Locate every blood parasite and identify its species.
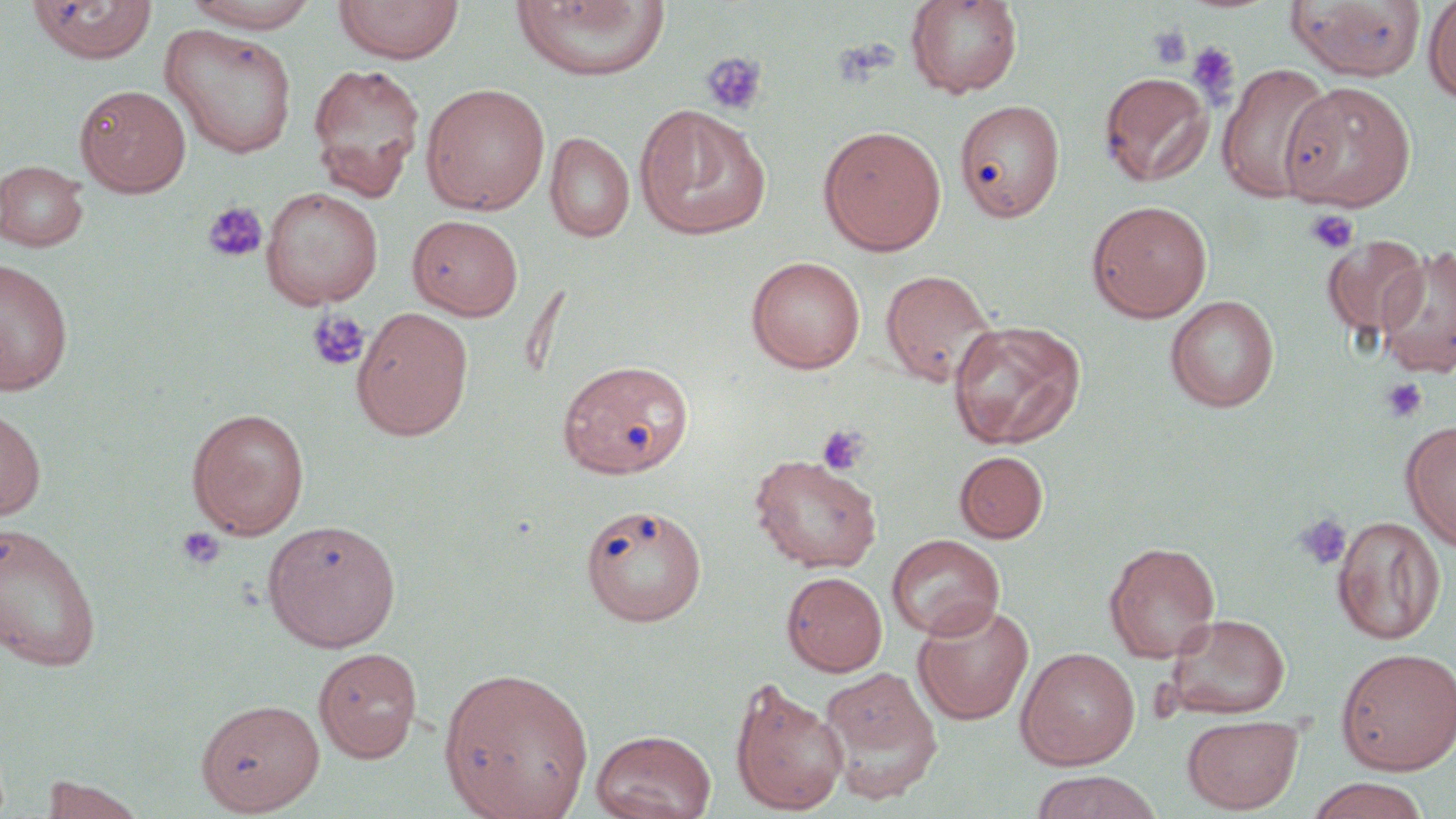

No blood parasites seen.

Summary:
  - Coordinate format: approximate bounding boxes as named x1/y1/x2/y2 corners in pixels
  - Uninfected red blood cell locations: (x1=28, y1=0, x2=157, y2=63), (x1=182, y1=0, x2=323, y2=32), (x1=332, y1=0, x2=464, y2=63), (x1=906, y1=0, x2=1022, y2=99), (x1=1287, y1=0, x2=1427, y2=81), (x1=511, y1=1, x2=670, y2=81), (x1=1423, y1=1, x2=1456, y2=103), (x1=159, y1=23, x2=299, y2=159), (x1=307, y1=62, x2=426, y2=199), (x1=1217, y1=63, x2=1336, y2=202), (x1=1099, y1=72, x2=1214, y2=187), (x1=1280, y1=81, x2=1416, y2=211), (x1=421, y1=83, x2=550, y2=216), (x1=75, y1=84, x2=191, y2=197), (x1=954, y1=99, x2=1065, y2=221), (x1=634, y1=105, x2=771, y2=240), (x1=818, y1=125, x2=947, y2=256), (x1=545, y1=131, x2=635, y2=243), (x1=0, y1=159, x2=90, y2=252), (x1=261, y1=187, x2=384, y2=309), (x1=1086, y1=199, x2=1212, y2=322), (x1=408, y1=214, x2=523, y2=320), (x1=1322, y1=235, x2=1428, y2=341), (x1=1376, y1=247, x2=1456, y2=379), (x1=746, y1=256, x2=866, y2=374), (x1=0, y1=257, x2=74, y2=397), (x1=879, y1=268, x2=999, y2=389), (x1=1165, y1=294, x2=1280, y2=412), (x1=352, y1=306, x2=474, y2=441), (x1=949, y1=320, x2=1086, y2=450), (x1=558, y1=359, x2=694, y2=479), (x1=0, y1=405, x2=46, y2=523), (x1=187, y1=407, x2=310, y2=538), (x1=1401, y1=419, x2=1456, y2=551), (x1=954, y1=451, x2=1048, y2=543), (x1=748, y1=453, x2=883, y2=574), (x1=581, y1=502, x2=707, y2=626), (x1=1332, y1=515, x2=1445, y2=645), (x1=262, y1=518, x2=402, y2=652), (x1=0, y1=520, x2=103, y2=671), (x1=887, y1=534, x2=1005, y2=640), (x1=1104, y1=542, x2=1220, y2=662), (x1=781, y1=571, x2=888, y2=676), (x1=912, y1=602, x2=1035, y2=726), (x1=1164, y1=613, x2=1291, y2=720), (x1=313, y1=646, x2=422, y2=763), (x1=1015, y1=646, x2=1140, y2=769), (x1=1335, y1=647, x2=1456, y2=775), (x1=439, y1=665, x2=595, y2=819), (x1=819, y1=666, x2=942, y2=802), (x1=730, y1=677, x2=849, y2=815), (x1=195, y1=698, x2=325, y2=815), (x1=1182, y1=715, x2=1303, y2=814), (x1=590, y1=729, x2=716, y2=819), (x1=1029, y1=771, x2=1162, y2=819), (x1=39, y1=775, x2=146, y2=818), (x1=1303, y1=777, x2=1431, y2=819)
  - Platelet locations: (x1=1148, y1=25, x2=1192, y2=70), (x1=1186, y1=42, x2=1240, y2=105), (x1=701, y1=51, x2=767, y2=116), (x1=202, y1=201, x2=268, y2=263), (x1=1305, y1=209, x2=1359, y2=254), (x1=306, y1=309, x2=370, y2=372), (x1=1381, y1=378, x2=1428, y2=422), (x1=816, y1=423, x2=870, y2=476), (x1=1294, y1=513, x2=1352, y2=571), (x1=176, y1=527, x2=225, y2=570)
  - Slide-level diagnosis: negative for blood parasites
  - Image size: 1456×819 pixels
  - Field of view: single
  - Magnification: 1000x
  - Preparation: thin blood film
  - Modality: light microscopy
  - Stain: May-Grünwald-Giemsa